Assess this cell for malaria.
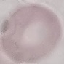
It is uninfected.

Summary:
  - Image type: automatically extracted cell patch, resized to 64 × 64 pixels
  - Preparation: thin blood film
  - Stain: Giemsa
  - Capture: smartphone camera at the microscope eyepiece